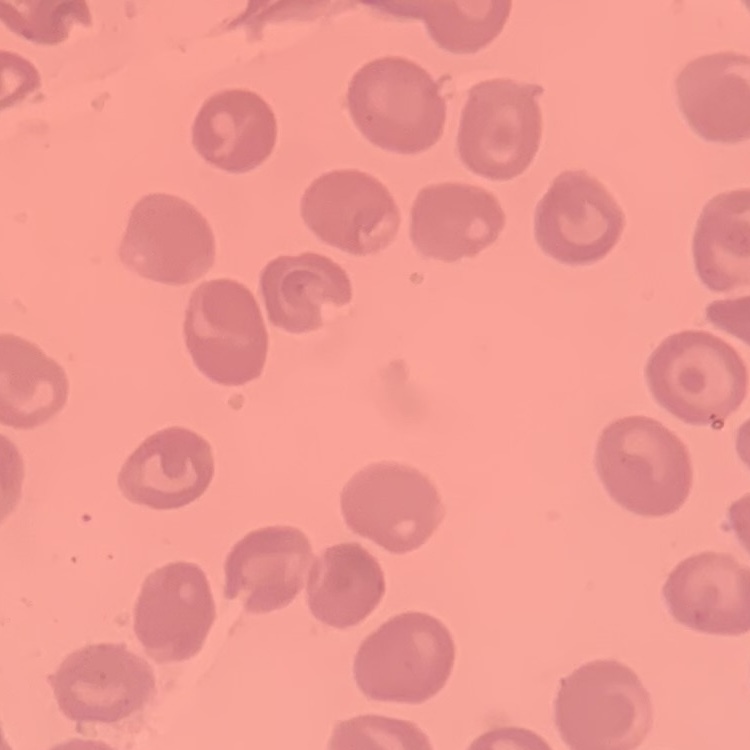
{
  "erythrocyte_morphology": "no rouleaux formation",
  "image_type": "square crop of a larger photomicrograph",
  "preparation": "thin peripheral smear",
  "stain": "Field's or Giemsa"
}